Describe the morphology of the red blood cells.
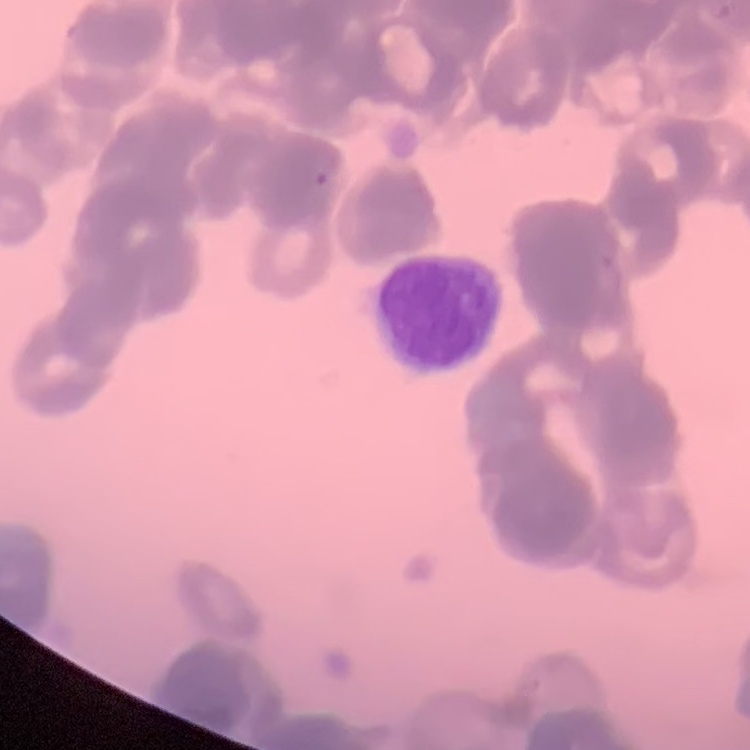
They show rouleaux formation.

stain = Field's or Giemsa
image type = square crop of a larger photomicrograph
preparation = thin blood film